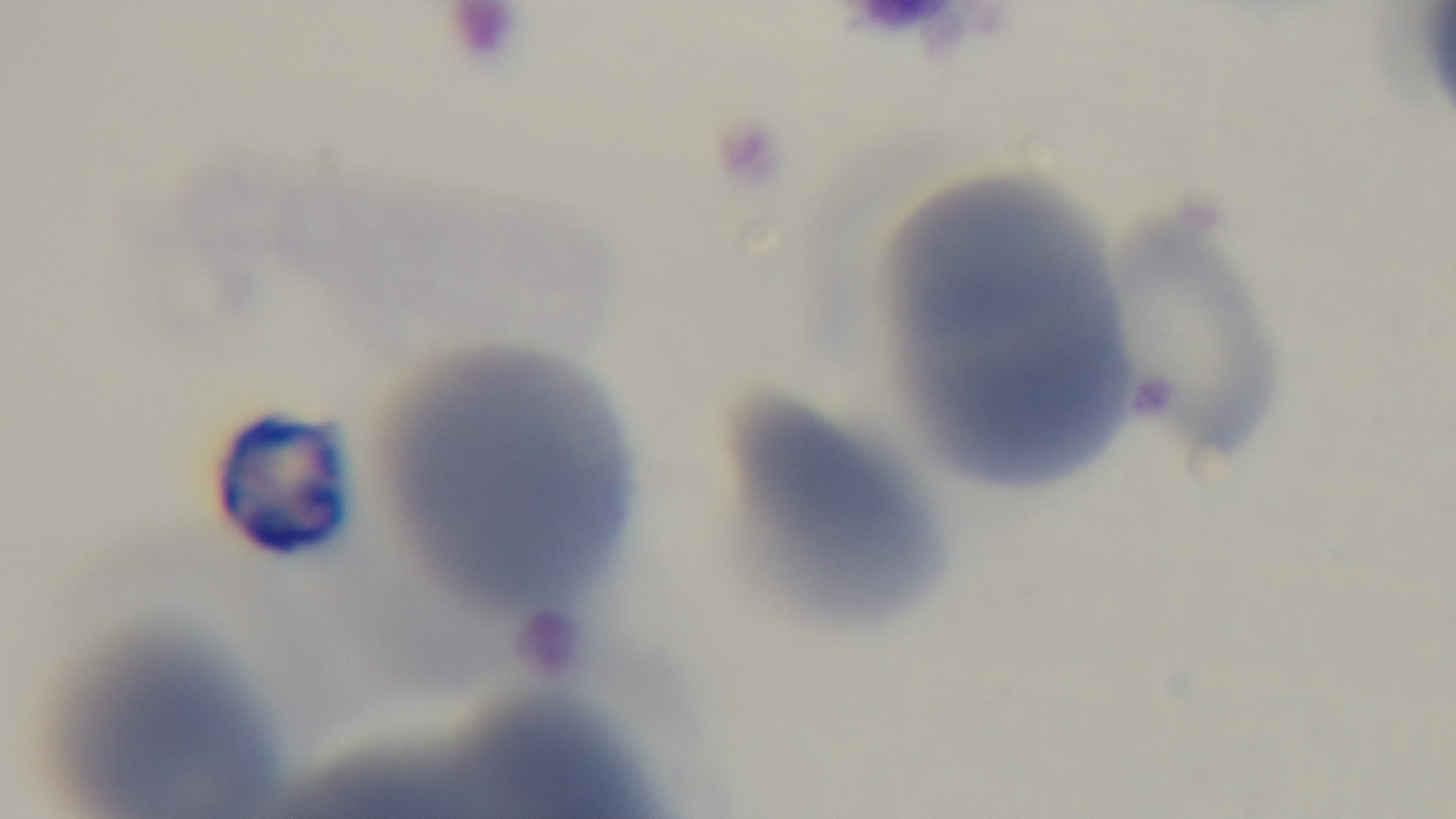
Summary:
  - Objective: 100x oil immersion
  - Modality: light microscopy
  - Stain: Giemsa
  - Malaria status: uninfected
  - Field of view: single
  - Preparation: thin smear
  - Capture: mounted 4K digital camera